Name the blood parasite species.
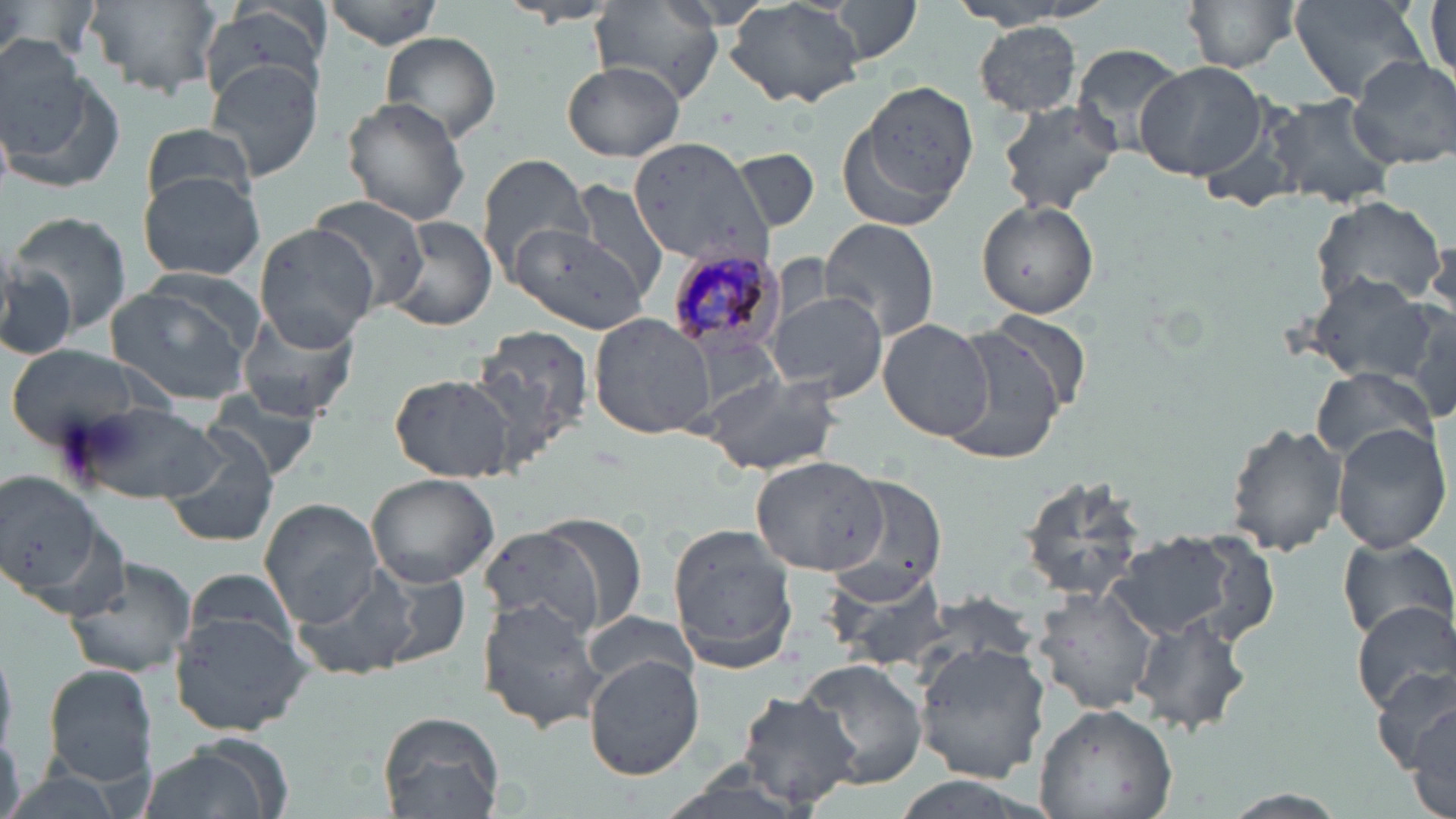

Plasmodium malariae.

Summary:
  - Coordinate format: approximate bounding boxes as [x1, y1, x2, y2] in pixels
  - Uninfected red blood cell locations: [85, 0, 223, 98], [322, 0, 444, 49], [653, 0, 782, 32], [725, 0, 864, 109], [822, 0, 926, 66], [1184, 0, 1298, 73], [1426, 0, 1455, 95], [1290, 1, 1430, 102], [201, 3, 330, 99], [501, 3, 621, 28], [591, 4, 726, 101], [973, 20, 1083, 115], [379, 32, 501, 145], [0, 37, 88, 155], [1070, 44, 1189, 159], [1293, 51, 1437, 204], [1347, 55, 1456, 171], [202, 56, 324, 181], [563, 59, 685, 162], [1134, 62, 1270, 181], [5, 69, 124, 195], [860, 81, 979, 206], [1266, 95, 1397, 209], [343, 96, 472, 226], [996, 100, 1120, 216], [139, 124, 261, 215], [628, 138, 776, 270], [732, 148, 820, 231], [477, 154, 593, 283], [139, 174, 263, 281], [563, 179, 670, 301], [1309, 193, 1445, 313], [307, 195, 432, 314], [976, 198, 1101, 319], [5, 211, 134, 334], [385, 217, 495, 331], [819, 219, 942, 343], [254, 223, 379, 350], [504, 227, 647, 332], [0, 261, 79, 359], [1306, 277, 1436, 385], [104, 278, 260, 404], [770, 293, 887, 399], [1404, 303, 1456, 424], [236, 309, 363, 424], [975, 311, 1090, 419], [587, 312, 716, 441], [878, 319, 995, 441], [470, 323, 593, 465], [940, 328, 1067, 465], [689, 329, 787, 420], [4, 344, 154, 451], [1312, 367, 1435, 465], [704, 372, 844, 477], [388, 373, 518, 483], [204, 391, 326, 485], [67, 398, 228, 507], [1225, 423, 1346, 557], [1332, 425, 1450, 552], [157, 430, 281, 548], [752, 454, 883, 572], [0, 470, 120, 610], [366, 472, 499, 587], [824, 472, 951, 604], [1019, 477, 1153, 602], [259, 499, 382, 627], [535, 514, 649, 634], [477, 524, 606, 642], [667, 524, 801, 671], [1105, 531, 1250, 645], [1338, 540, 1455, 641], [63, 554, 198, 682], [291, 565, 424, 682], [187, 568, 299, 663], [1034, 589, 1156, 715], [477, 599, 605, 733], [1350, 601, 1456, 715], [170, 610, 313, 738], [583, 610, 699, 690], [1134, 612, 1253, 736], [915, 641, 1050, 780], [585, 652, 705, 780], [795, 658, 927, 788], [41, 663, 159, 789], [1375, 668, 1455, 775], [734, 689, 862, 810], [1033, 700, 1176, 819], [1412, 704, 1454, 814], [377, 710, 504, 819], [135, 739, 289, 819]
  - Plasmodium malariae-infected red blood cell locations: [663, 250, 788, 357]
  - Modality: optical microscopy
  - Image size: 1456×819 pixels
  - Magnification: 1000x
  - Stain: May-Grünwald-Giemsa
  - Field of view: one of a larger specimen
  - Preparation: thin blood film